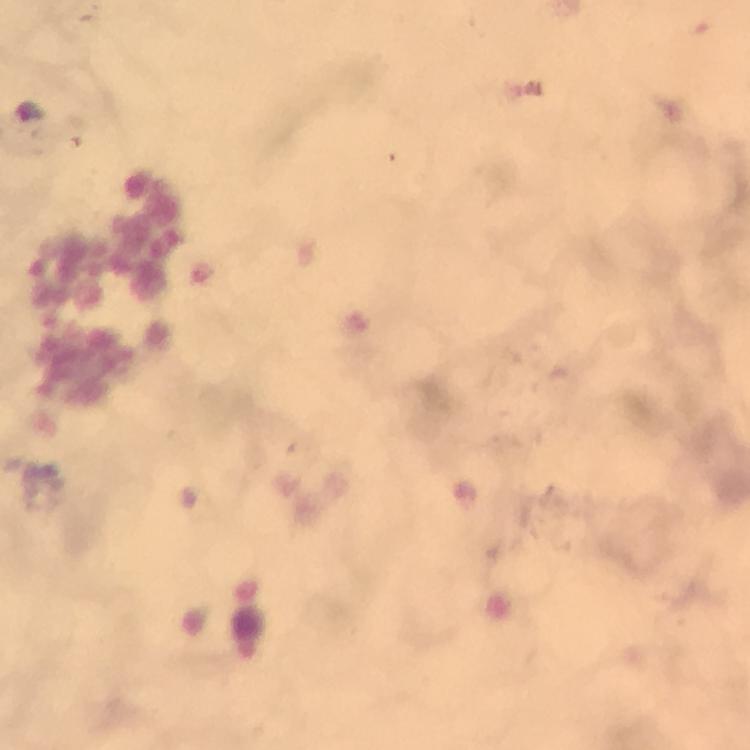
context = from a diagnostic examination for malaria
immersion oil = applied
magnification = 100x
image size = 750×750 pixels
capture = smartphone mounted on the microscope
stain = Giemsa
preparation = thick blood smear
malaria parasite locations = approximate object centers, in pixels from the top-left corner: (x=30, y=109)
cropped from = a single field of view